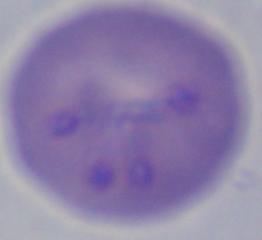
Summary:
  - Identification: Babesia
  - Modality: micrograph
  - Magnification: 1000x